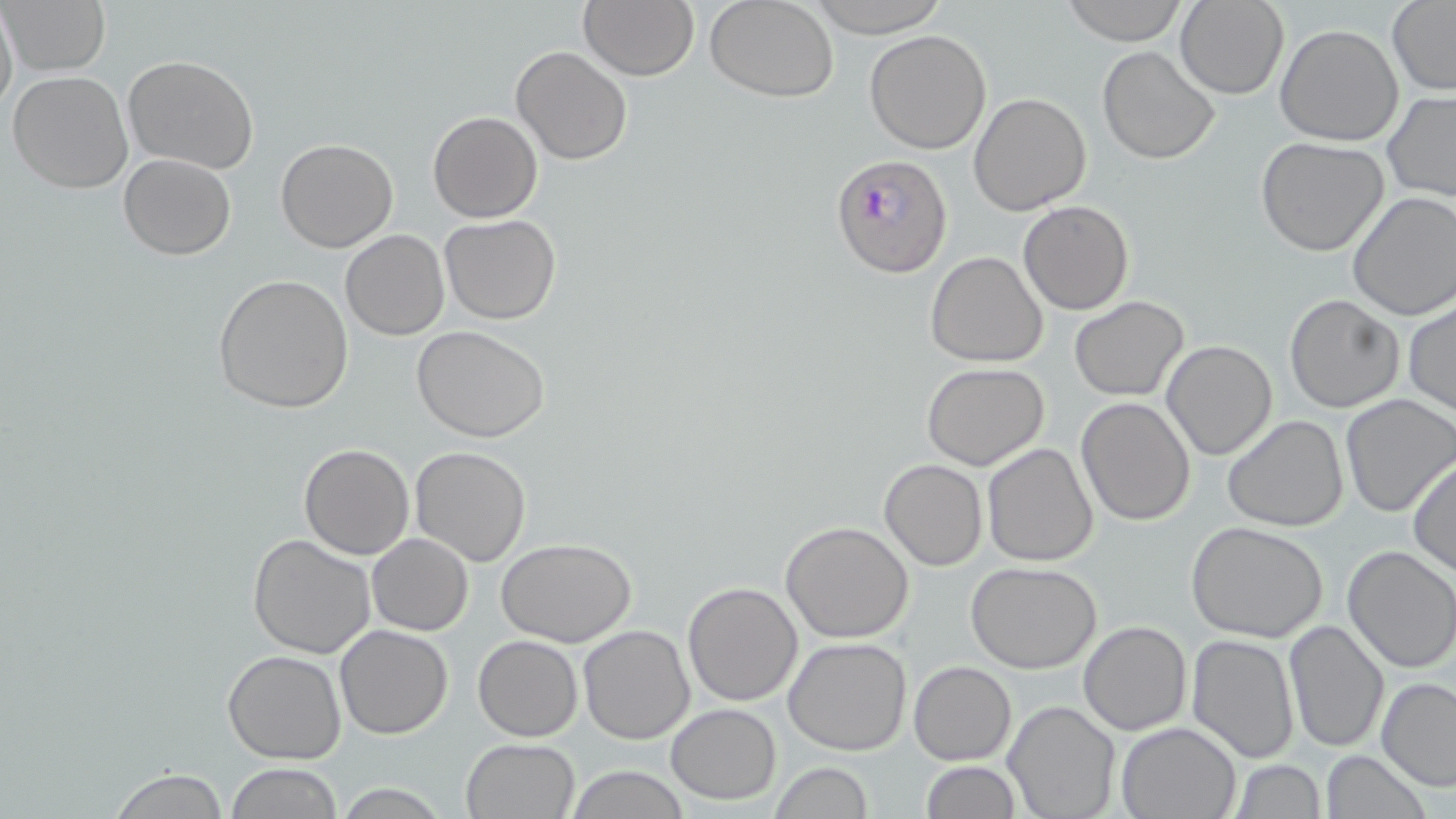
Plasmodium falciparum-infected red blood cell locations = approximate bounding boxes as (x1,y1)-(x2,y2) corner pairs in pixels: (831,154)-(952,279)
slide-level diagnosis = Plasmodium falciparum
uninfected red blood cell locations = approximate bounding boxes as (x1,y1)-(x2,y2) corner pairs in pixels: (2,0)-(112,75), (578,0)-(701,81), (706,0)-(840,102), (802,0)-(948,37), (1059,0)-(1190,44), (0,1)-(18,121), (1176,1)-(1287,99), (1387,2)-(1456,93), (1275,24)-(1405,147), (865,30)-(992,154), (510,45)-(633,166), (1097,46)-(1221,165), (122,54)-(261,173), (6,72)-(132,195), (1383,91)-(1456,202), (968,92)-(1093,216), (427,111)-(543,223), (1256,137)-(1389,257), (277,139)-(399,253), (118,153)-(236,259), (1347,191)-(1456,321), (1018,201)-(1135,316), (440,214)-(561,325), (340,231)-(450,340), (925,251)-(1049,367), (211,274)-(354,413), (1284,293)-(1404,413), (1068,296)-(1190,401), (1404,298)-(1455,416), (412,326)-(552,442), (1160,340)-(1279,461), (921,362)-(1051,471), (1339,395)-(1455,517), (1077,397)-(1196,524), (1222,415)-(1349,533), (299,443)-(415,560), (982,443)-(1101,567), (410,446)-(531,566), (1407,457)-(1456,579), (880,458)-(987,571), (781,521)-(914,644), (1189,524)-(1330,643), (246,534)-(377,659), (367,534)-(474,636), (496,538)-(637,645), (1342,545)-(1456,673), (966,562)-(1101,674), (681,581)-(803,705), (1282,620)-(1390,755), (1079,621)-(1192,735), (334,624)-(454,739), (578,624)-(696,745), (1187,633)-(1300,764), (473,634)-(583,742), (783,636)-(912,755), (224,649)-(347,765), (908,660)-(1016,766), (1377,677)-(1456,791), (1004,700)-(1120,819), (666,703)-(782,803), (1115,720)-(1242,818), (461,739)-(581,819), (1319,751)-(1432,819), (770,761)-(872,818), (919,761)-(1019,818), (1228,761)-(1326,818), (224,764)-(342,818), (562,766)-(694,819), (104,769)-(231,818), (331,783)-(454,817)
preparation = thin blood film
stain = May-Grünwald-Giemsa
magnification = 1000x
image size = 1456×819 pixels
field of view = one of a larger specimen
modality = light microscopy